Classify this cell by malaria status.
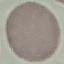
Uninfected.

preparation: thin blood film
image_type: automatically extracted cell patch, resized to 64 × 64 pixels
stain: Giemsa
capture: smartphone through the microscope eyepiece